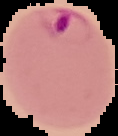
Summary:
  - Result: Plasmodium parasites identified
  - Preparation: thin blood smear
  - Image size: 118×136 pixels
  - Image type: segmented cell region with the area outside set to black